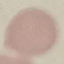
Summary:
  - Malaria status: uninfected
  - Capture: smartphone camera at the microscope eyepiece
  - Stain: Giemsa
  - Preparation: thin blood film
  - Image type: cell patch, automatically extracted from a larger field of view and resized to 64 × 64 pixels